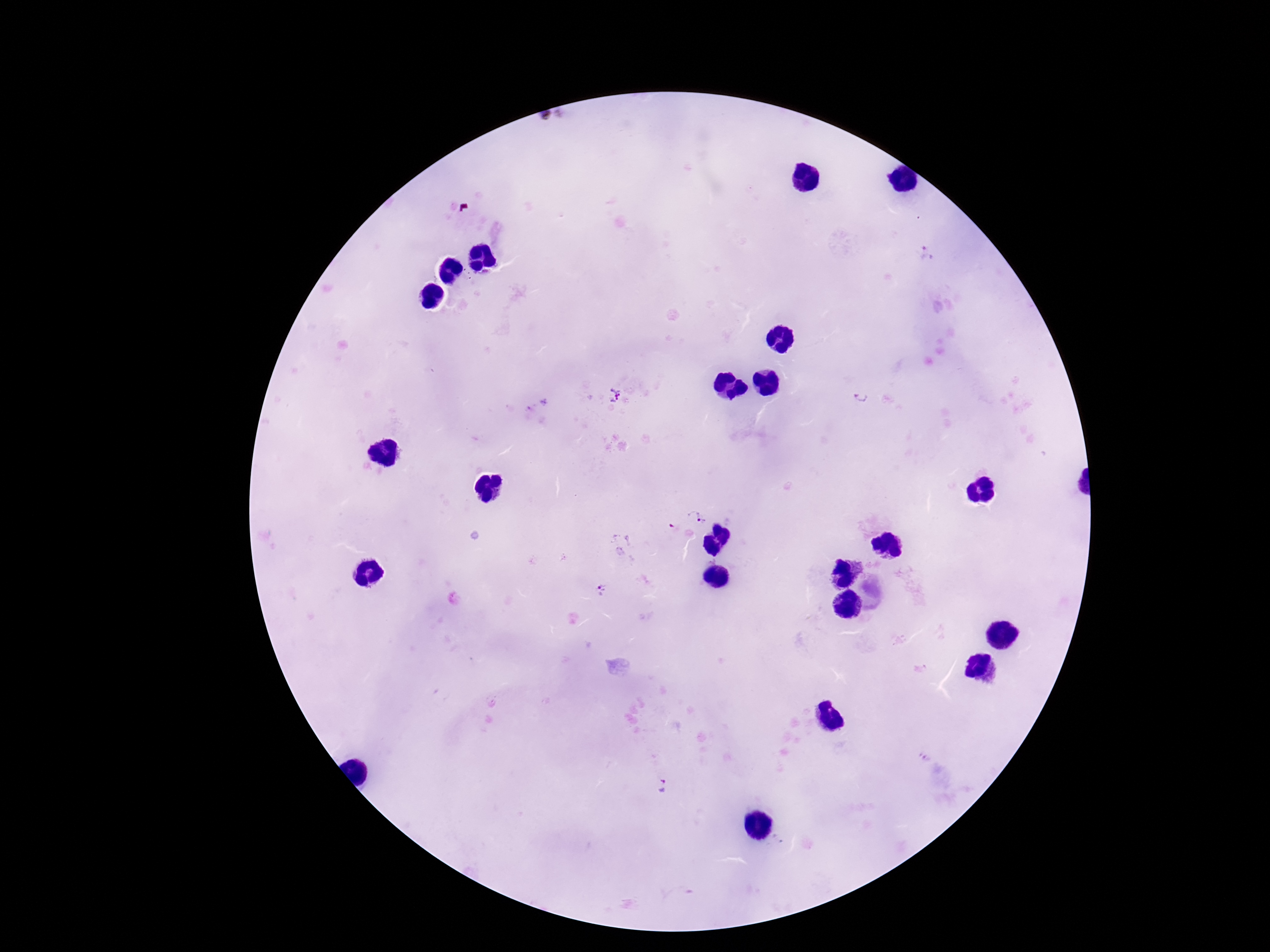
capture: smartphone camera through the microscope eyepiece
stain: Giemsa
field_of_view: single
magnification: 100x
plasmodium_parasite_locations: 'approximate centers as {x, y} in pixels: {926, 254}, {614, 394}, {861, 397}, {697, 517}, {601, 589}, {664, 785}'
preparation: thick peripheral-blood smear
patient_malaria_status: infected
image_size: 1270×952 pixels